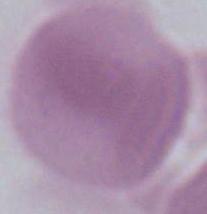
magnification = 1000x
identification = erythrocyte
modality = photomicrograph